Find the red blood cells that are infected with P. falciparum, and any of indeterminate infection status.
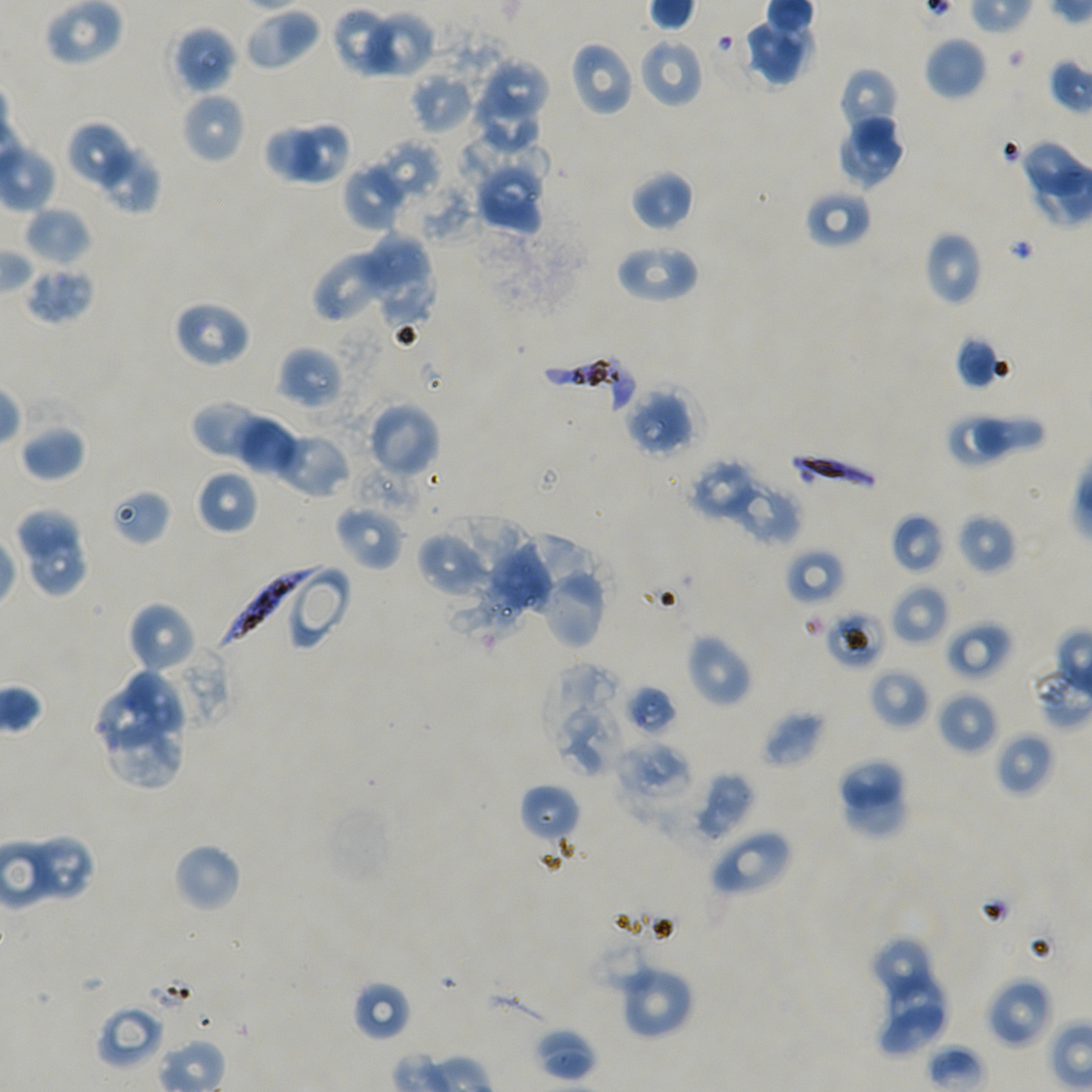
Approximate bounding boxes as (x1, y1, x2, y2) in pixels. Not every red blood cell is marked.
Infected red blood cells: (538, 354, 634, 413), (788, 455, 880, 500), (216, 564, 326, 653).
Red blood cells of indeterminate infection status: (110, 488, 171, 546), (824, 608, 885, 670), (623, 683, 678, 735).

Locations of uninfected red blood cells: (44, 0, 124, 65), (242, 7, 322, 72), (331, 7, 401, 77), (360, 10, 436, 79), (741, 17, 812, 87), (172, 25, 238, 95), (924, 36, 987, 101), (638, 37, 704, 109), (570, 41, 636, 117), (485, 58, 549, 120), (838, 67, 900, 145), (409, 69, 476, 134), (473, 87, 538, 153), (180, 91, 247, 164), (835, 115, 905, 189), (297, 124, 348, 183), (69, 125, 134, 185), (264, 126, 321, 183), (456, 128, 549, 202), (1020, 138, 1092, 198), (370, 140, 443, 204), (105, 145, 156, 211), (472, 156, 549, 235), (342, 160, 408, 233), (630, 169, 694, 232), (805, 187, 872, 250), (24, 206, 93, 268), (923, 230, 983, 306), (359, 234, 431, 289), (615, 242, 700, 304), (313, 245, 397, 325), (359, 255, 438, 329), (22, 264, 94, 325), (172, 299, 251, 369), (954, 335, 1006, 390), (276, 346, 344, 410), (623, 387, 695, 457), (191, 400, 271, 462), (365, 401, 441, 479), (972, 411, 1046, 459), (949, 416, 1006, 468), (237, 417, 299, 477), (20, 422, 87, 483), (274, 430, 352, 498), (687, 459, 761, 520), (195, 469, 259, 535), (723, 479, 805, 545), (335, 505, 404, 571), (19, 507, 79, 557), (956, 511, 1016, 575), (891, 513, 945, 574), (437, 515, 524, 593), (416, 530, 491, 598), (510, 534, 600, 625), (32, 536, 88, 594), (484, 543, 552, 611), (785, 547, 847, 607), (290, 566, 352, 651), (536, 568, 607, 651), (889, 583, 949, 647), (126, 600, 197, 675), (945, 619, 1013, 680), (685, 631, 753, 708), (543, 663, 630, 778), (869, 668, 930, 729), (126, 670, 187, 734), (101, 688, 161, 751), (936, 691, 1000, 755), (761, 708, 824, 769), (106, 723, 183, 790), (994, 731, 1055, 797), (615, 742, 695, 811), (837, 757, 903, 807), (685, 771, 754, 844), (848, 780, 908, 837), (520, 784, 580, 843), (708, 829, 793, 897), (26, 835, 95, 901), (172, 842, 242, 913), (869, 936, 931, 1000), (617, 962, 695, 1040), (888, 972, 943, 1032), (986, 976, 1054, 1048), (351, 979, 413, 1042), (879, 1001, 946, 1056), (95, 1004, 164, 1071), (533, 1027, 597, 1081). One field from this slide. Oil immersion, 100x objective (numerical aperture 1.45). Image is 1092×1092 pixels. Giemsa stain. Donor blood group A+/O+. P. falciparum strain NF54 maintained in static in-vitro culture. Thin blood smear.